Classify this cell by malaria status.
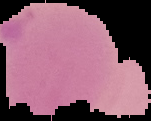

Parasitized.

image size = 151×121 pixels
image type = segmented cell region on a black background
preparation = thin blood film